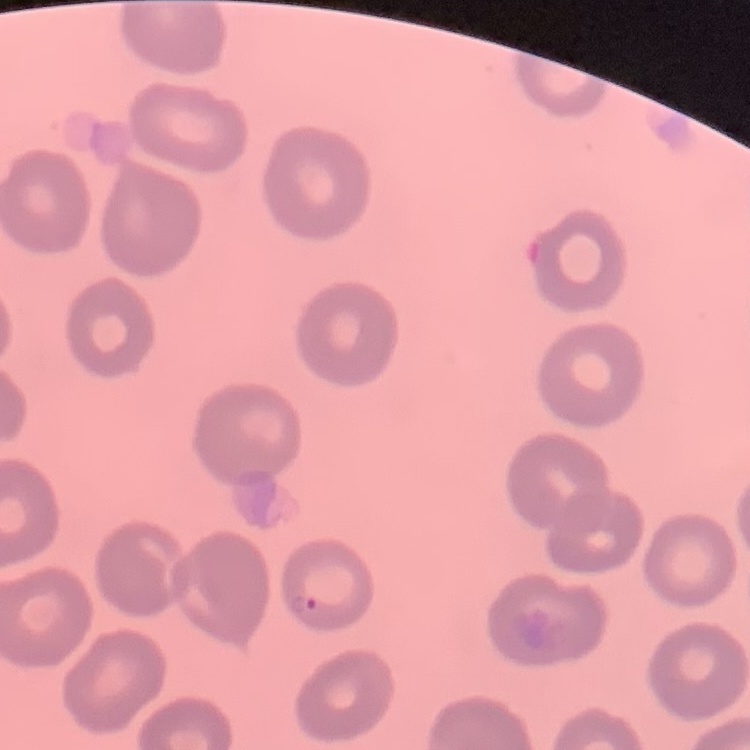
{
  "red_blood_cell_morphology": "no rouleaux formation",
  "image_type": "square crop of a larger photomicrograph",
  "preparation": "thin blood smear",
  "stain": "Field's or Giemsa"
}